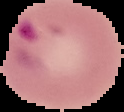
Summary:
  - Malaria status: parasitized
  - Image size: 124×112 pixels
  - Preparation: thin blood film
  - Image type: segmented cell region with the area outside set to black